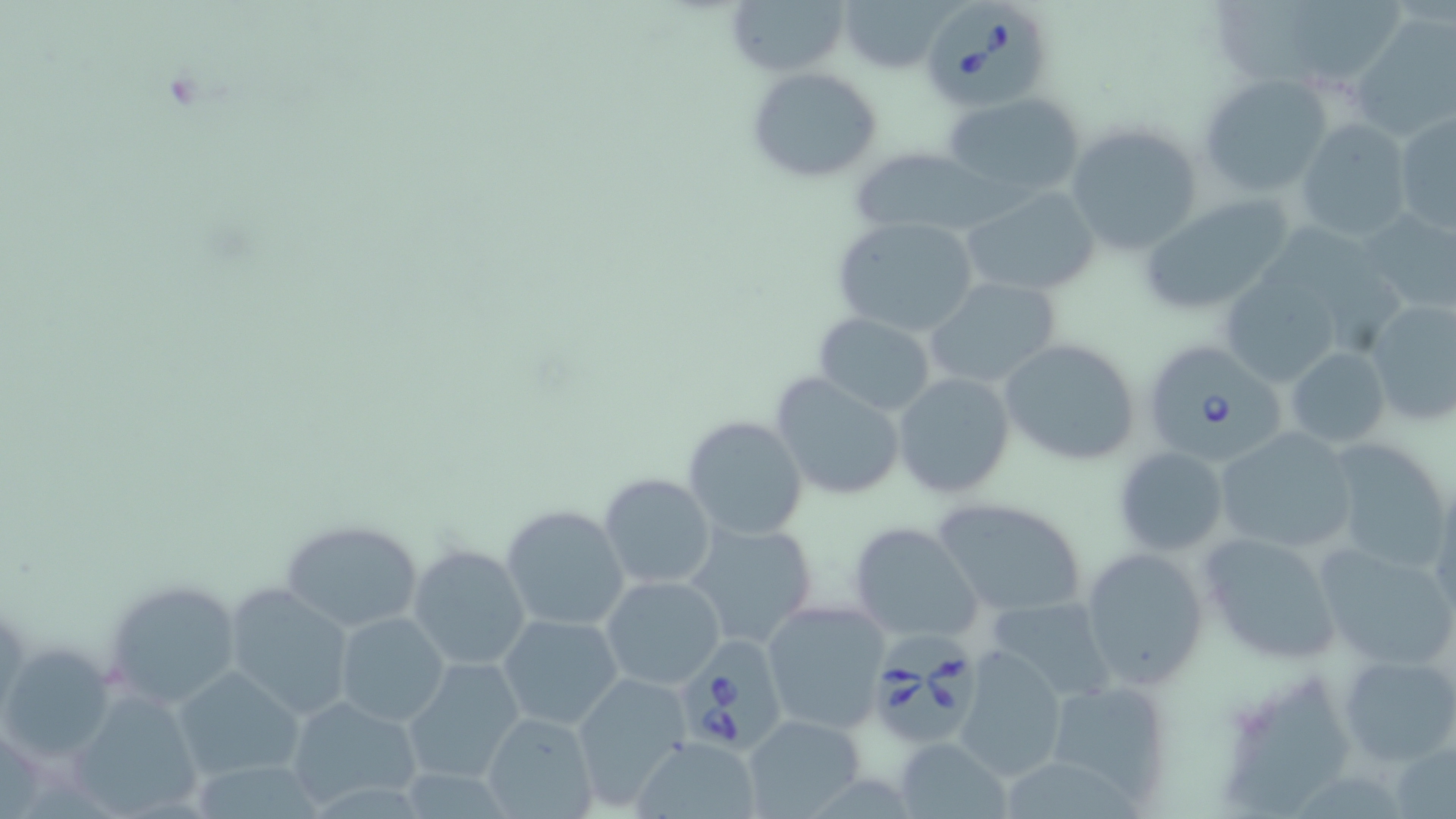

{
  "slide_level_diagnosis": "Babesia divergens",
  "uninfected_red_blood_cell_locations": "approximate bounding boxes as [x1, y1, x2, y2] in pixels: [724, 0, 852, 77], [837, 0, 952, 74], [1352, 13, 1456, 141], [748, 67, 885, 183], [1197, 74, 1331, 197], [941, 93, 1087, 197], [1393, 109, 1455, 236], [1294, 119, 1413, 242], [1067, 124, 1203, 256], [849, 147, 1005, 237], [959, 184, 1103, 299], [1137, 195, 1296, 316], [1361, 207, 1456, 314], [831, 216, 979, 337], [921, 276, 1064, 390], [1221, 278, 1343, 386], [1363, 297, 1456, 428], [812, 312, 935, 415], [1000, 338, 1143, 466], [1284, 346, 1391, 448], [892, 372, 1016, 498], [770, 373, 907, 501], [682, 415, 809, 541], [1214, 427, 1359, 557], [1322, 436, 1455, 573], [1112, 446, 1229, 555], [597, 473, 716, 592], [931, 496, 1090, 617], [501, 504, 630, 633], [278, 518, 423, 633], [847, 520, 986, 645], [685, 521, 819, 652], [1198, 529, 1344, 665], [1314, 539, 1456, 670], [408, 544, 531, 671], [1081, 545, 1209, 691], [600, 575, 726, 690], [101, 577, 240, 709], [224, 583, 356, 720], [983, 596, 1116, 703], [761, 599, 891, 736], [335, 613, 448, 727], [497, 613, 626, 732], [951, 644, 1069, 782], [3, 646, 114, 763], [1338, 653, 1456, 768], [404, 659, 526, 782], [174, 667, 304, 780], [571, 676, 692, 809], [1042, 677, 1177, 809], [68, 689, 204, 819], [285, 694, 423, 811], [481, 709, 600, 819], [742, 713, 866, 819], [631, 736, 763, 819], [895, 736, 1014, 819]",
  "babesia_divergens_infected_red_blood_cell_locations": "approximate bounding boxes as [x1, y1, x2, y2] in pixels: [922, 3, 1048, 116], [1148, 349, 1289, 466], [873, 631, 990, 750], [673, 643, 776, 749]",
  "stain": "May-Grünwald-Giemsa",
  "field_of_view": "one of a larger specimen",
  "preparation": "thin blood film",
  "magnification": "1000x",
  "modality": "light microscopy",
  "image_size": "1456×819 pixels"
}